Identify the parasite.
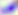
This is Toxoplasma gondii.

{
  "magnification": "400x",
  "modality": "micrograph"
}